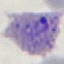

Malaria status: parasitized. Giemsa stain. Thin smear of blood. Cell patch, automatically extracted from a larger field of view and resized to 64 × 64 pixels. Acquired by smartphone through the microscope eyepiece.